Name the parasite shown.
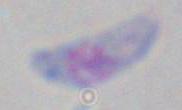

Toxoplasma gondii.

modality: micrograph
magnification: 1000x